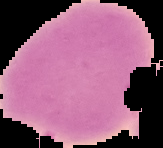

preparation = thin blood smear
image size = 163×148 pixels
image type = segmented cell region with the area outside set to black
malaria status = uninfected